Classify this cell by malaria status.
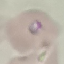
Parasitized.

Acquired by smartphone through the microscope eyepiece. Giemsa-stained preparation. Cell patch, automatically extracted from a larger field of view and resized to 64 × 64 pixels. Thin blood smear.